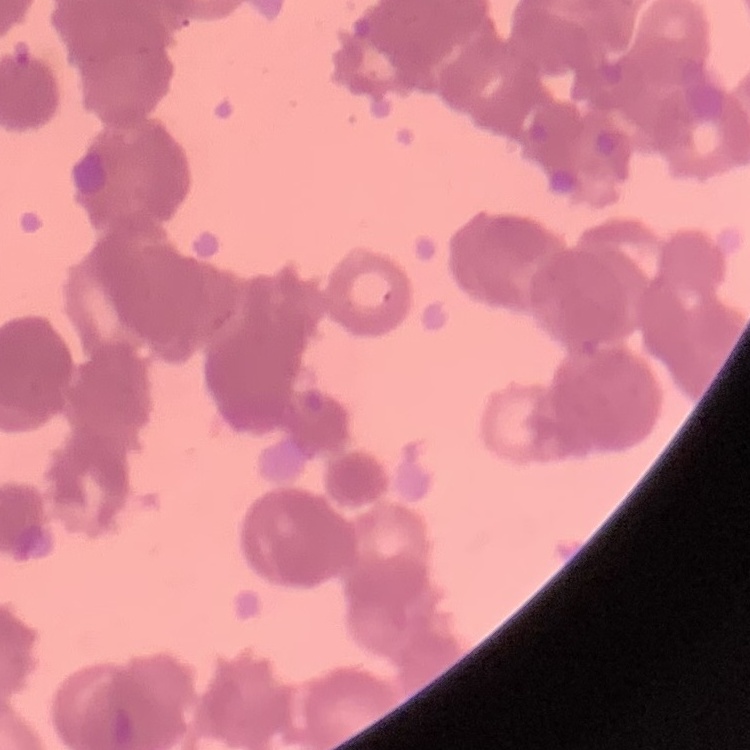

erythrocyte morphology = rouleaux formation
image type = one tile cut from a larger photomicrograph
stain = Field's or Giemsa
preparation = thin blood smear